Locate every blood parasite and identify its species.
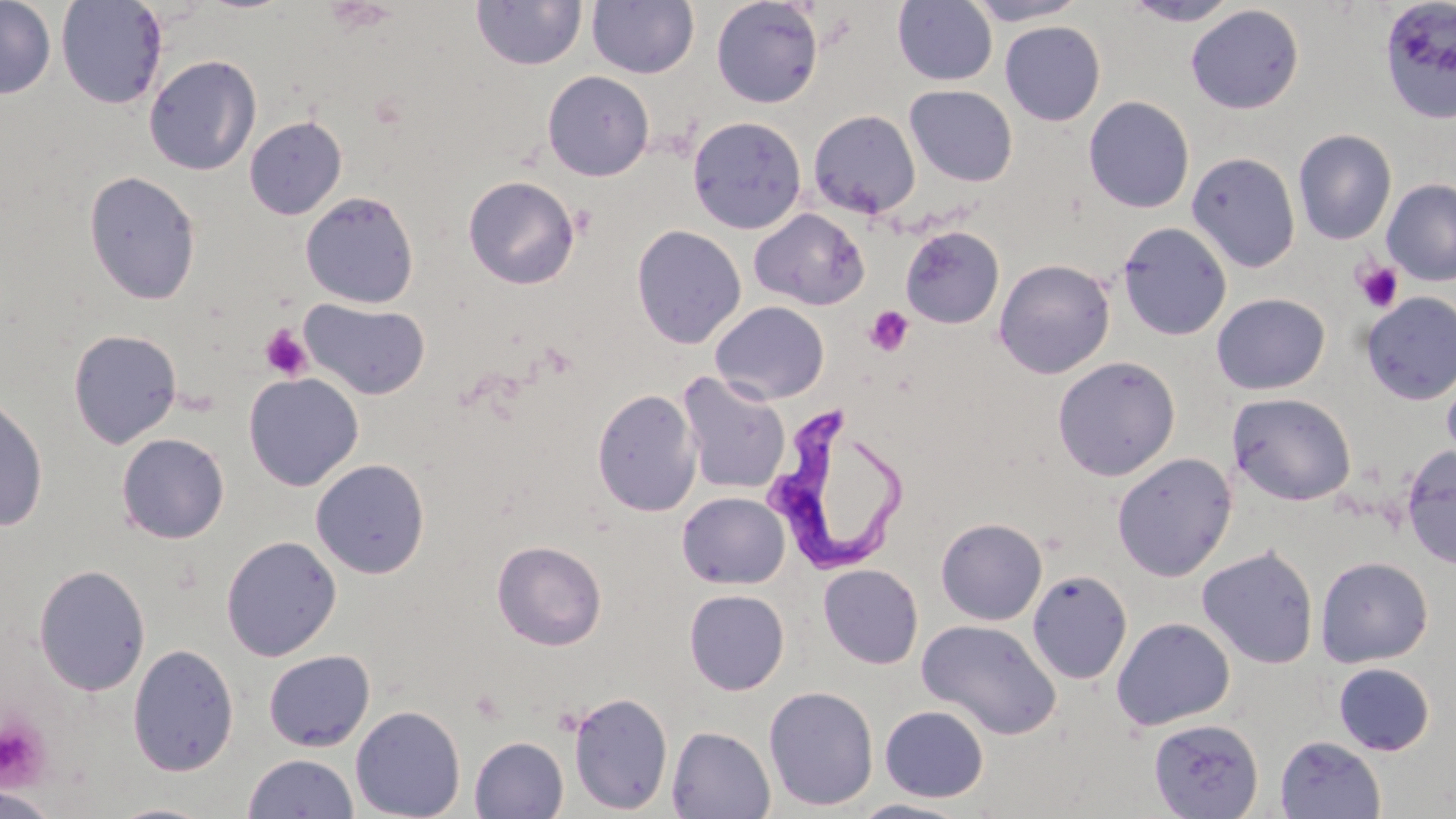
Approximate bounding boxes as (x1, y1, x2, y2) in pixels.
Trypanosoma brucei: (760, 407, 907, 576).
No Plasmodium falciparum, Plasmodium ovale, Plasmodium malariae, Plasmodium vivax, or Babesia divergens observed.

slide_level_diagnosis: Trypanosoma brucei
magnification: 1000x
stain: May-Grünwald-Giemsa
preparation: thin blood smear
modality: optical microscopy
platelet_locations: 'approximate bounding boxes as (x1, y1, x2, y2) in pixels: (1353, 260, 1404, 313), (865, 306, 914, 356), (259, 324, 313, 382), (0, 714, 53, 791)'
field_of_view: single
image_size: 1456×819 pixels
uninfected_red_blood_cell_locations: 'approximate bounding boxes as (x1, y1, x2, y2) in pixels: (0, 0, 56, 99), (56, 0, 167, 110), (711, 0, 823, 108), (893, 0, 997, 86), (962, 0, 1088, 25), (1120, 0, 1242, 26), (1377, 0, 1456, 126), (471, 1, 587, 71), (587, 1, 699, 79), (1185, 5, 1305, 114), (999, 21, 1105, 126), (143, 54, 262, 176), (542, 70, 654, 181), (904, 85, 1018, 187), (1083, 96, 1195, 214), (808, 110, 921, 219), (244, 116, 347, 220), (687, 116, 807, 234), (1293, 129, 1397, 245), (1186, 152, 1301, 273), (83, 170, 202, 306), (463, 175, 580, 289), (1376, 178, 1456, 402), (1382, 179, 1456, 287), (300, 191, 420, 308), (749, 207, 869, 311), (1117, 222, 1232, 342), (631, 224, 746, 349), (901, 225, 1005, 329), (994, 258, 1115, 378), (1360, 291, 1456, 405), (1211, 293, 1330, 395), (299, 298, 431, 401), (710, 301, 830, 404), (68, 328, 183, 448), (1052, 356, 1180, 481), (1441, 368, 1456, 469), (677, 371, 791, 495), (244, 372, 364, 491), (592, 388, 701, 516), (0, 392, 49, 532), (1227, 392, 1357, 506), (116, 433, 230, 543), (1401, 445, 1456, 569), (1112, 452, 1237, 581), (310, 458, 430, 579), (676, 491, 790, 589), (935, 517, 1047, 625), (221, 535, 341, 661), (492, 539, 607, 650), (1197, 545, 1319, 669), (1315, 556, 1433, 667), (818, 563, 923, 669), (34, 564, 150, 696), (1027, 570, 1133, 685), (684, 589, 789, 695), (1111, 617, 1235, 731), (917, 618, 1061, 740), (127, 643, 240, 776), (263, 650, 375, 751), (1333, 662, 1435, 755), (763, 685, 879, 811), (568, 692, 674, 815), (350, 705, 466, 819), (878, 705, 990, 802), (1148, 718, 1263, 818), (666, 726, 776, 818), (1274, 735, 1386, 819), (469, 736, 569, 818), (242, 753, 360, 818), (0, 788, 62, 819), (848, 798, 973, 818), (103, 801, 218, 819)'